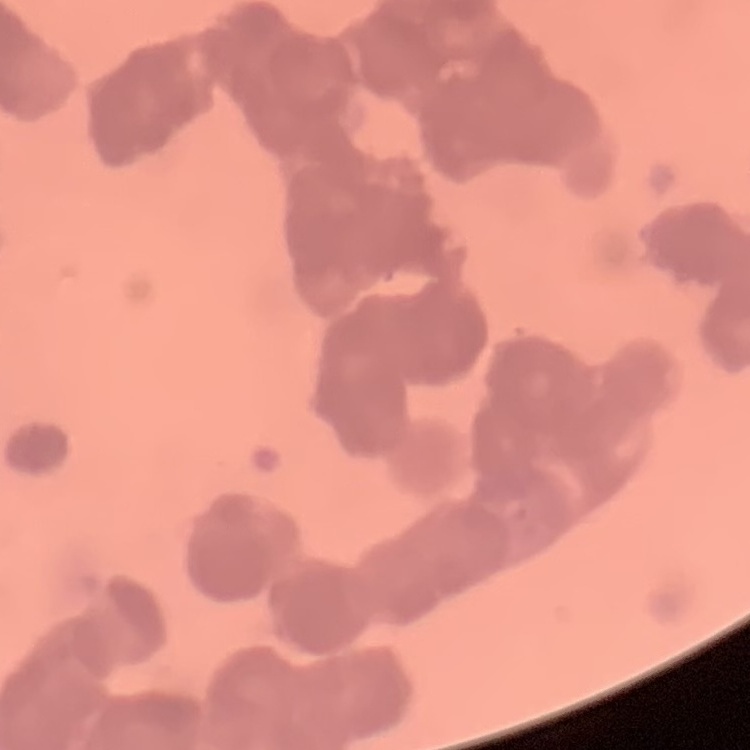

Summary:
  - Erythrocyte morphology: rouleaux formation
  - Image type: one tile cut from a larger photomicrograph
  - Stain: Field's or Giemsa
  - Preparation: thin blood smear